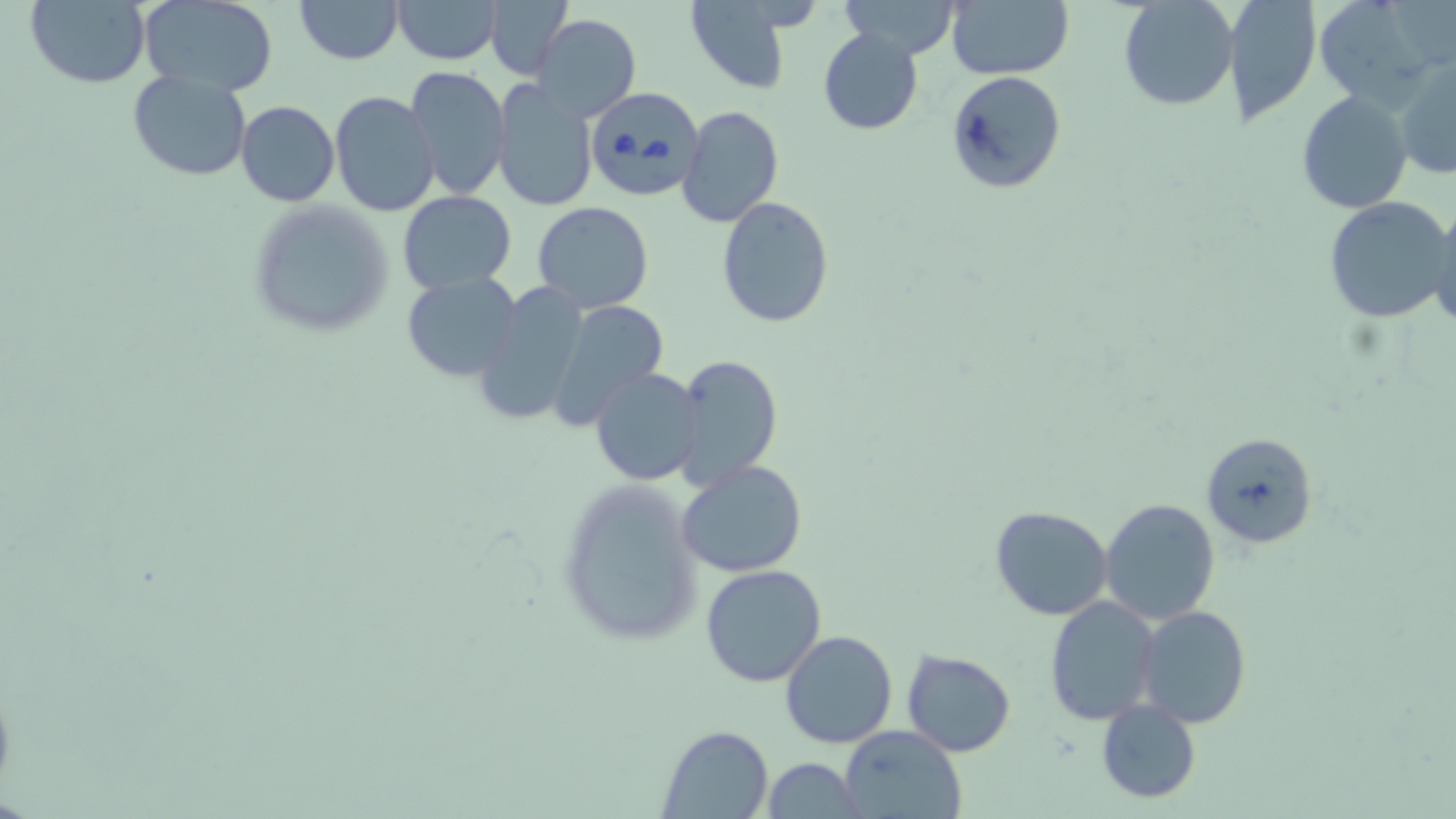
{
  "slide_level_diagnosis": "Babesia divergens",
  "preparation": "thin blood film",
  "babesia_divergens_infected_red_blood_cell_locations": "approximate bounding boxes as [x1, y1, x2, y2] in pixels: [587, 86, 705, 200]",
  "field_of_view": "one of a larger specimen",
  "stain": "May-Grünwald-Giemsa",
  "magnification": "1000x",
  "uninfected_red_blood_cell_locations": "approximate bounding boxes as [x1, y1, x2, y2] in pixels: [24, 0, 151, 88], [139, 0, 278, 96], [296, 0, 402, 64], [392, 0, 503, 65], [486, 0, 574, 82], [683, 0, 801, 91], [946, 0, 1073, 80], [1118, 0, 1238, 110], [1222, 0, 1321, 125], [1313, 0, 1441, 107], [836, 1, 965, 61], [533, 13, 641, 123], [818, 28, 923, 135], [1395, 60, 1456, 179], [404, 65, 510, 199], [947, 69, 1066, 194], [127, 70, 253, 180], [489, 78, 598, 212], [1296, 89, 1414, 213], [329, 91, 440, 217], [236, 100, 339, 205], [679, 105, 784, 229], [399, 192, 515, 292], [716, 196, 835, 327], [1323, 196, 1454, 324], [247, 200, 391, 337], [533, 201, 654, 312], [1429, 204, 1455, 328], [402, 271, 523, 381], [471, 284, 588, 429], [544, 298, 672, 428], [671, 353, 783, 489], [590, 367, 705, 484], [1200, 431, 1319, 549], [676, 460, 808, 578], [554, 478, 704, 648], [1099, 497, 1219, 625], [989, 506, 1114, 621], [700, 564, 827, 687], [1045, 597, 1159, 724], [1136, 605, 1252, 730], [780, 630, 897, 749], [900, 649, 1016, 756], [1096, 698, 1201, 803], [658, 726, 773, 817], [840, 727, 967, 819], [759, 759, 863, 818]",
  "image_size": "1456×819 pixels",
  "modality": "light microscopy"
}